Give the extent of all uninfected red blood cells.
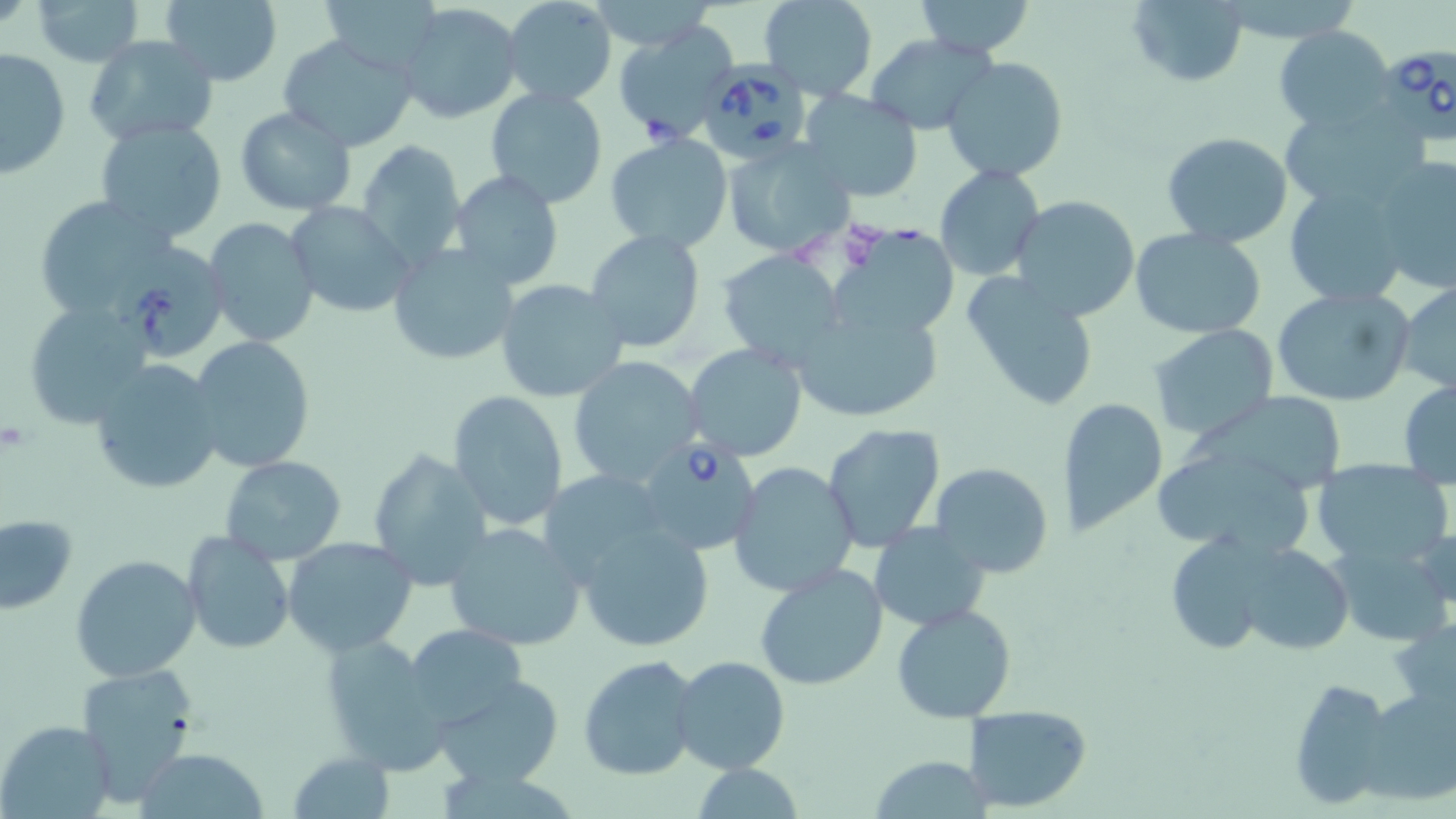

Approximate bounding boxes as (x1,y1)-(x2,y2) corner pairs in pixels.
Uninfected red blood cells: (29,0)-(143,67), (160,0)-(283,87), (318,0)-(443,75), (500,0)-(618,108), (757,0)-(877,100), (913,0)-(1037,60), (1125,0)-(1250,88), (399,5)-(519,124), (612,22)-(739,145), (1273,26)-(1398,131), (278,34)-(420,151), (84,35)-(222,147), (863,35)-(997,135), (0,47)-(71,177), (942,55)-(1069,183), (484,87)-(609,209), (799,90)-(924,202), (1280,105)-(1425,211), (234,107)-(359,216), (93,119)-(230,244), (604,132)-(734,254), (1159,132)-(1294,246), (356,140)-(469,271), (722,141)-(854,259), (1370,153)-(1456,293), (934,165)-(1044,280), (450,169)-(565,293), (1284,181)-(1413,306), (32,194)-(183,323), (1011,195)-(1143,322), (283,202)-(414,318), (205,217)-(320,347), (829,222)-(956,340), (585,229)-(705,352), (1129,229)-(1266,340), (112,241)-(230,361), (387,243)-(520,367), (718,250)-(847,369), (961,271)-(1099,412), (495,278)-(630,403), (1397,280)-(1456,395), (1271,286)-(1414,407), (21,300)-(157,428), (791,304)-(944,424), (1149,325)-(1279,442), (186,336)-(316,474), (684,343)-(810,462), (566,357)-(704,488), (86,358)-(225,495), (1398,378)-(1456,487), (1193,380)-(1350,489), (446,391)-(570,532), (1062,396)-(1170,538), (822,422)-(947,552), (366,448)-(491,593), (220,454)-(346,566), (1154,458)-(1310,555), (1308,458)-(1455,568), (727,462)-(859,597), (930,462)-(1055,577), (537,470)-(673,587), (1,514)-(77,615), (574,520)-(713,652), (443,521)-(589,652), (870,525)-(993,631), (181,530)-(296,654), (1162,530)-(1289,656), (283,537)-(417,656), (1330,539)-(1455,646), (1232,541)-(1358,655), (70,555)-(202,681), (754,563)-(889,691), (891,603)-(1018,721), (403,624)-(525,727), (320,632)-(449,773), (578,653)-(702,781), (671,654)-(790,775), (73,661)-(199,804), (433,674)-(565,786), (1286,677)-(1396,808), (1360,686)-(1456,805), (963,704)-(1093,811), (0,719)-(116,819), (137,748)-(268,818), (287,750)-(395,818), (870,755)-(993,819).

slide-level diagnosis = Babesia divergens
stain = May-Grünwald-Giemsa
magnification = 1000x
field of view = single
Babesia divergens-infected red blood cell locations = approximate bounding boxes as (x1,y1)-(x2,y2) corner pairs in pixels: (1381,42)-(1455,150), (704,57)-(808,164), (633,438)-(760,557)
image size = 1456×819 pixels
preparation = thin blood smear
modality = light microscopy